Assess this cell for malaria.
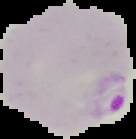

It is parasitized.

image type = segmented cell region on a black background
preparation = thin blood smear
image size = 136×139 pixels